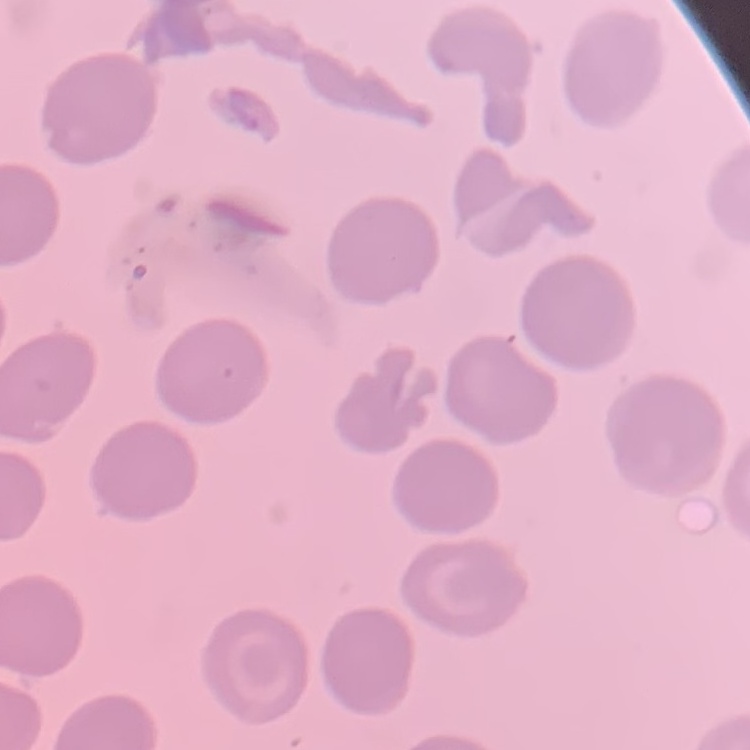
The erythrocytes exhibit no rouleaux formation. Thin peripheral smear. Field's or Giemsa stain. Square crop of a larger photomicrograph.